Locate and identify every blood parasite.
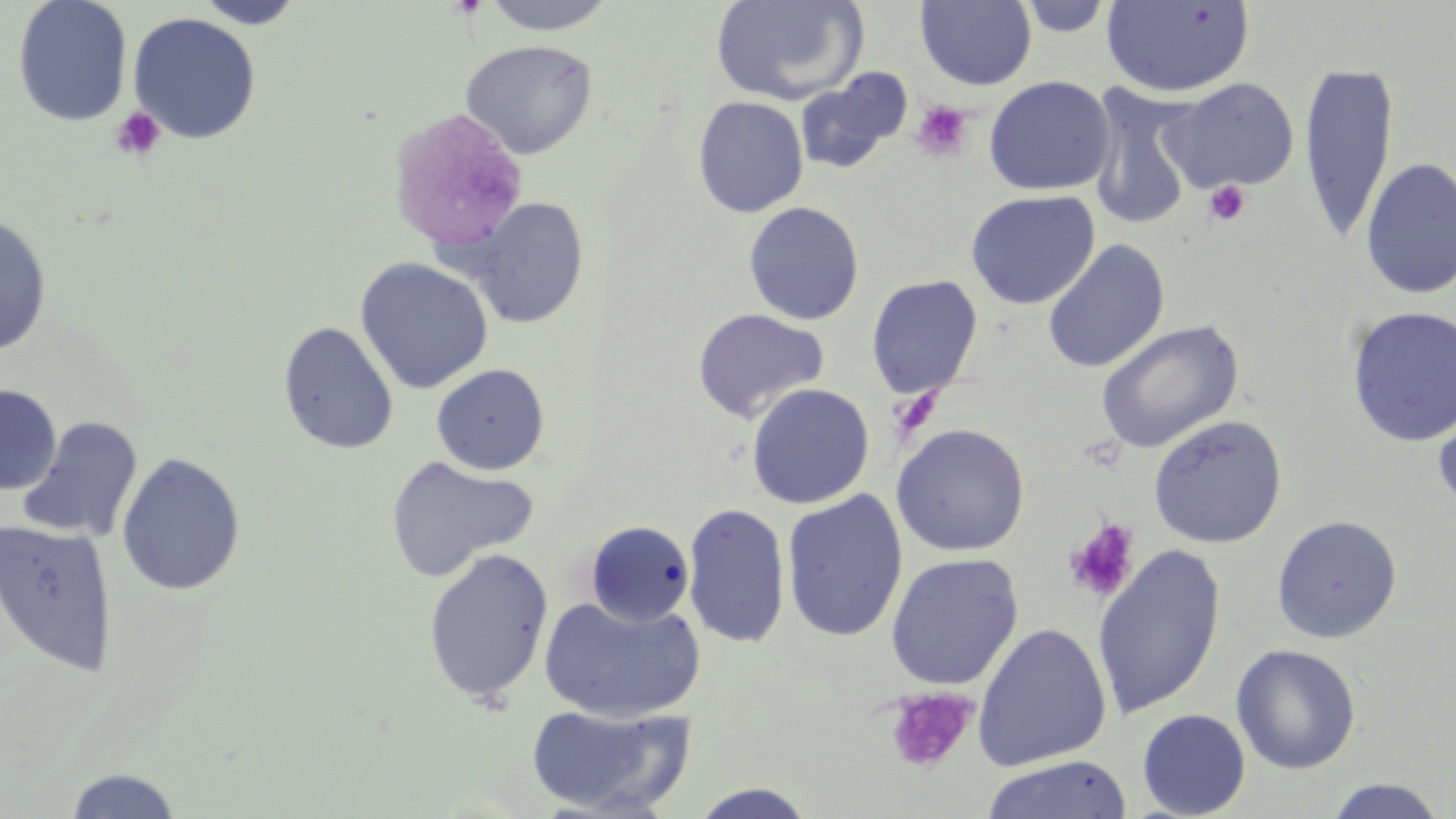

No blood parasites observed.

Approximate bounding boxes as [x1, y1, x2, y2] in pixels. Platelet locations: [911, 100, 974, 161], [110, 107, 166, 161], [1204, 180, 1251, 226], [1063, 518, 1141, 602], [883, 685, 978, 774]. Uninfected red blood cell locations: [12, 0, 133, 126], [193, 0, 307, 29], [479, 0, 620, 35], [709, 0, 867, 106], [1016, 0, 1116, 37], [916, 1, 1037, 90], [1101, 1, 1255, 99], [127, 12, 262, 144], [459, 39, 598, 160], [1298, 60, 1399, 244], [795, 68, 912, 176], [983, 76, 1115, 196], [1161, 77, 1300, 194], [1088, 84, 1201, 231], [693, 96, 809, 218], [1360, 158, 1456, 300], [965, 189, 1101, 309], [465, 196, 590, 329], [743, 201, 864, 326], [0, 213, 53, 357], [1043, 240, 1169, 373], [354, 257, 493, 394], [866, 275, 983, 400], [1346, 306, 1456, 447], [692, 308, 829, 423], [1095, 319, 1245, 454], [278, 321, 399, 454], [431, 363, 550, 475], [746, 382, 874, 509], [0, 384, 61, 496], [1432, 398, 1456, 520], [1148, 415, 1287, 548], [17, 417, 144, 543], [891, 424, 1029, 556], [116, 452, 246, 596], [384, 453, 538, 582], [781, 489, 908, 643], [682, 502, 791, 648], [1271, 515, 1403, 644], [0, 519, 118, 678], [585, 520, 695, 626], [1092, 544, 1227, 719], [422, 548, 554, 704], [885, 553, 1023, 690], [539, 594, 705, 722], [973, 623, 1112, 771], [1230, 644, 1361, 775], [524, 702, 693, 816], [1137, 708, 1251, 818], [981, 755, 1133, 819], [63, 768, 184, 818], [1323, 778, 1449, 819], [687, 783, 820, 818]. Slide-level diagnosis: negative for blood parasites. Single field of view. Image is 1456×819 pixels. Light microscopy. 1000x magnification. Thin blood film. May-Grünwald-Giemsa stain.